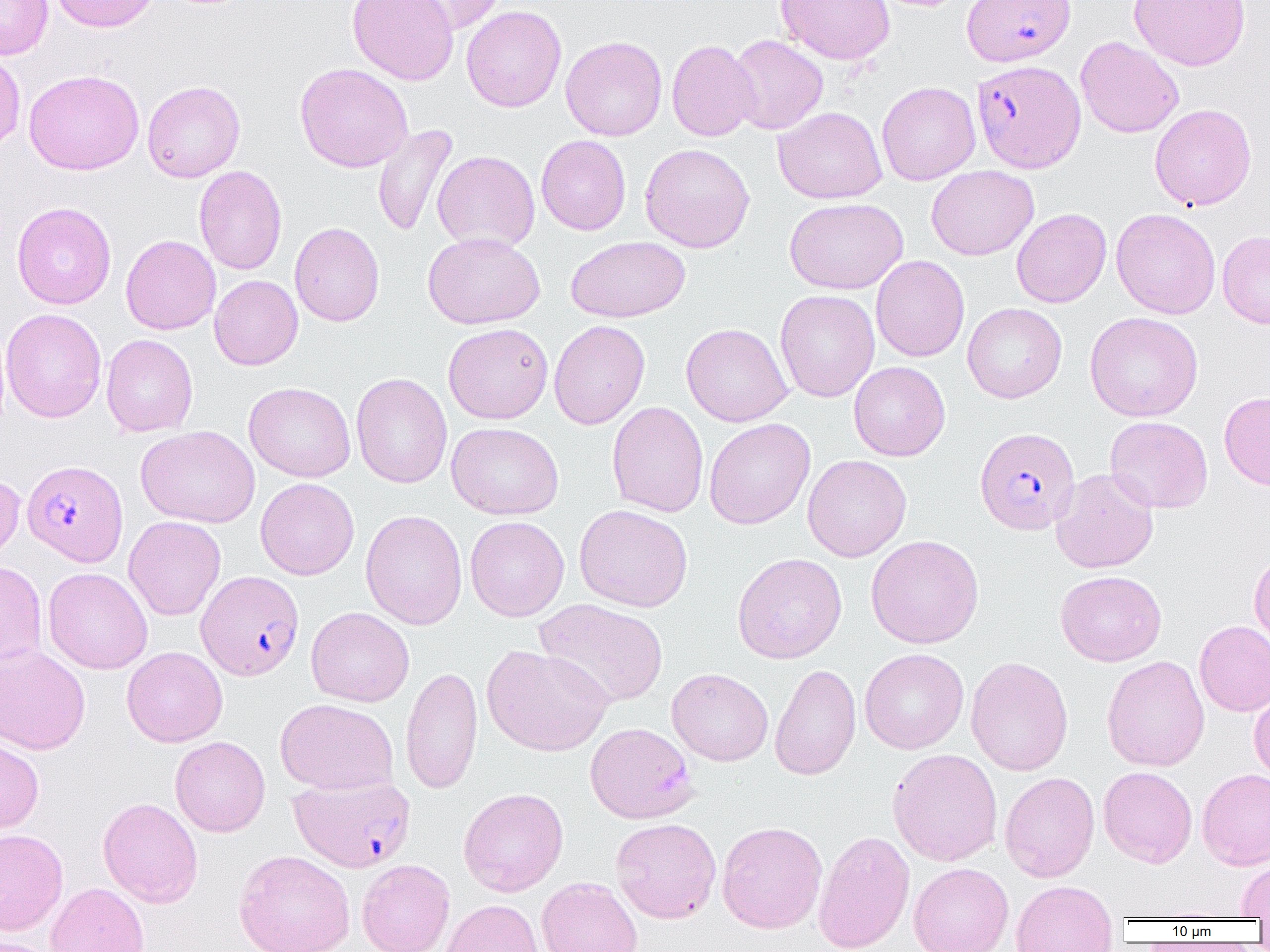

slide_level_diagnosis: Plasmodium falciparum
field_of_view: one of a larger specimen
preparation: thin blood film
plasmodium_falciparum_infected_red_blood_cell_locations_subset: 'approximate bounding boxes as (x1,y1)-(x2,y2) corner pairs in pixels: (961,0)-(1076,67), (971,60)-(1085,172), (974,426)-(1080,535), (22,459)-(128,566), (195,570)-(305,681), (288,774)-(415,872)'
magnification: 1000x
uninfected_red_blood_cell_locations_subset: 'approximate bounding boxes as (x1,y1)-(x2,y2) corner pairs in pixels: (0,0)-(53,60), (49,0)-(160,32), (346,0)-(459,85), (395,0)-(510,35), (775,0)-(895,65), (1129,0)-(1250,70), (461,5)-(567,113), (727,34)-(828,134), (560,35)-(667,141), (1075,36)-(1184,138), (667,39)-(760,142), (0,49)-(25,153), (294,63)-(414,172), (23,69)-(144,175), (142,80)-(245,182), (877,81)-(980,186), (1149,103)-(1257,210), (774,106)-(887,204), (372,124)-(459,237), (536,134)-(631,235), (640,143)-(755,253), (432,151)-(540,253), (194,165)-(287,275), (926,165)-(1039,260), (784,197)-(908,294), (11,202)-(116,309), (1011,208)-(1111,308), (1111,208)-(1221,319), (289,222)-(385,327), (1217,230)-(1270,329), (423,232)-(545,329), (120,235)-(221,335), (567,235)-(690,322), (870,255)-(969,362), (209,275)-(303,370), (774,290)-(880,402), (962,302)-(1067,403), (1,308)-(107,423), (1084,311)-(1203,421), (549,319)-(650,430), (443,322)-(554,424), (681,322)-(793,427), (693,323)-(799,527), (101,334)-(198,437), (849,361)-(950,461), (351,373)-(452,489), (244,381)-(356,482), (1219,391)-(1270,490), (607,401)-(708,518), (1105,415)-(1213,513), (704,418)-(815,529), (446,422)-(564,519), (135,426)-(260,528), (802,453)-(912,562), (1050,468)-(1159,573), (0,470)-(25,566), (256,477)-(359,580), (574,504)-(693,612), (360,509)-(468,630), (123,516)-(225,621), (465,516)-(569,621), (865,534)-(984,649), (1249,549)-(1270,651), (732,552)-(847,663), (0,561)-(47,670), (42,567)-(153,674), (1055,570)-(1167,667), (533,598)-(668,707), (306,606)-(415,707), (1194,620)-(1270,716), (0,643)-(91,755), (482,644)-(613,756), (122,646)-(228,747), (859,648)-(969,754), (1102,655)-(1210,772), (965,656)-(1073,776), (770,663)-(861,781), (400,665)-(483,794), (667,667)-(773,766), (1249,686)-(1270,784), (275,698)-(398,795), (170,736)-(270,837), (0,737)-(44,835), (888,748)-(1003,866), (1098,766)-(1197,868), (1197,768)-(1270,869), (999,771)-(1099,882), (458,788)-(568,896), (98,797)-(203,908), (610,817)-(721,923), (717,821)-(827,934), (0,828)-(68,936), (813,830)-(915,952), (233,849)-(355,952), (1236,856)-(1270,920), (357,859)-(455,952), (909,862)-(1013,952), (536,876)-(643,952), (1011,880)-(1118,952), (45,882)-(149,952), (440,899)-(543,952), (1,936)-(58,952)'
image_size: 1270×952 pixels
modality: light microscopy